Assess this cell for malaria.
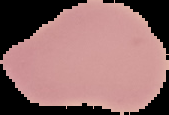

It is uninfected.

Summary:
  - Image size: 169×115 pixels
  - Image type: segmented cell region with the area outside set to black
  - Preparation: thin blood film